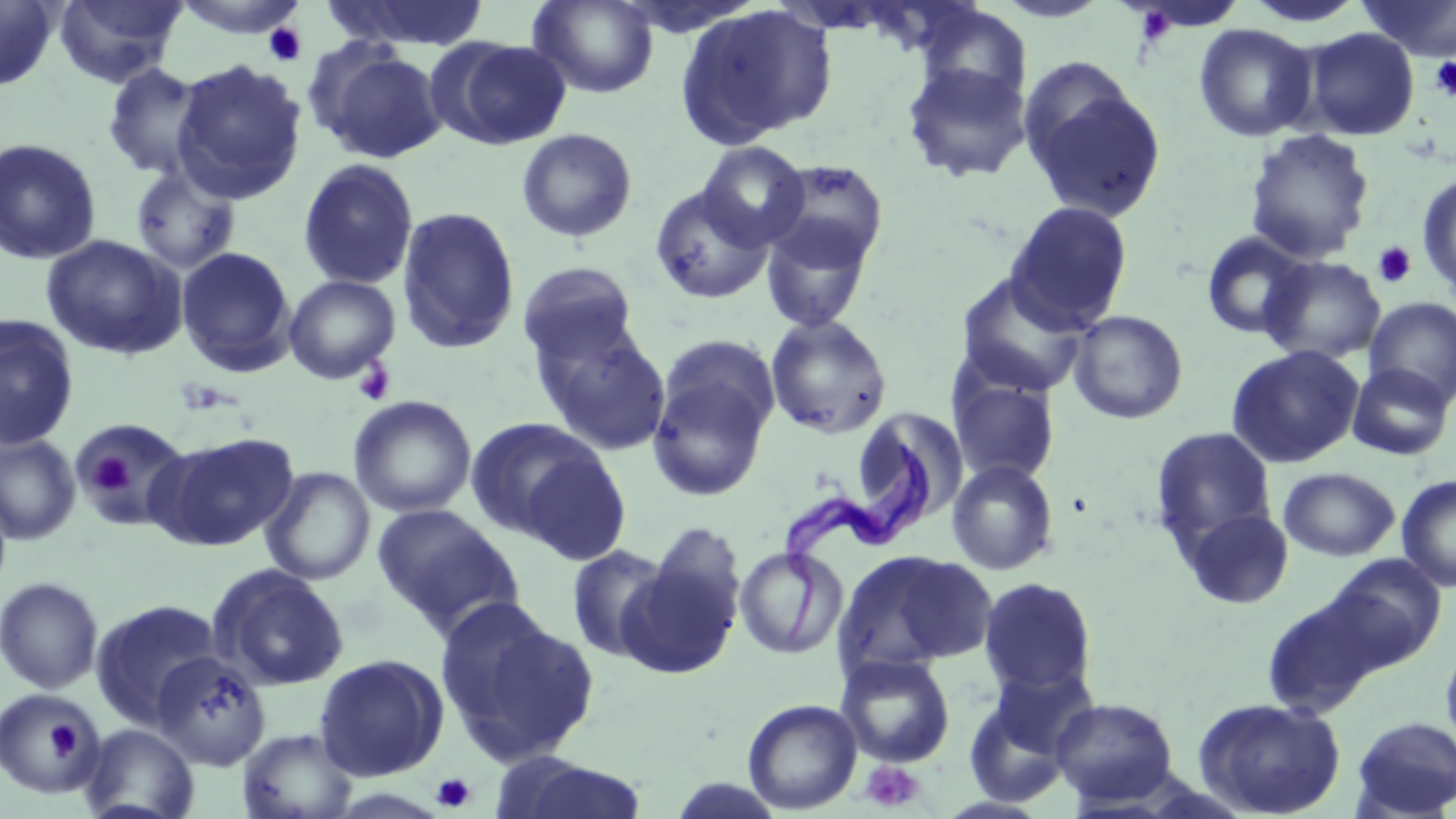

slide_level_diagnosis: Trypanosoma brucei
preparation: thin blood smear
uninfected_red_blood_cell_locations: 'approximate bounding boxes as named x1/y1/x2/y2 corners in pixels: (x1=0, y1=0, x2=59, y2=91), (x1=52, y1=0, x2=187, y2=88), (x1=170, y1=0, x2=311, y2=39), (x1=321, y1=0, x2=492, y2=51), (x1=527, y1=0, x2=659, y2=98), (x1=992, y1=0, x2=1111, y2=23), (x1=1243, y1=0, x2=1367, y2=29), (x1=1360, y1=0, x2=1456, y2=62), (x1=676, y1=3, x2=838, y2=148), (x1=915, y1=4, x2=1032, y2=106), (x1=1193, y1=24, x2=1318, y2=142), (x1=1297, y1=27, x2=1420, y2=141), (x1=440, y1=38, x2=572, y2=149), (x1=308, y1=42, x2=447, y2=164), (x1=172, y1=59, x2=307, y2=203), (x1=901, y1=62, x2=1032, y2=184), (x1=102, y1=63, x2=208, y2=181), (x1=1022, y1=79, x2=1166, y2=222), (x1=516, y1=128, x2=638, y2=243), (x1=1244, y1=128, x2=1375, y2=264), (x1=0, y1=138, x2=102, y2=265), (x1=697, y1=141, x2=811, y2=250), (x1=297, y1=159, x2=419, y2=290), (x1=764, y1=159, x2=890, y2=271), (x1=130, y1=165, x2=241, y2=275), (x1=1417, y1=172, x2=1456, y2=301), (x1=649, y1=184, x2=774, y2=305), (x1=1004, y1=200, x2=1133, y2=331), (x1=396, y1=206, x2=521, y2=355), (x1=759, y1=218, x2=875, y2=333), (x1=1200, y1=232, x2=1310, y2=339), (x1=41, y1=234, x2=187, y2=360), (x1=176, y1=246, x2=297, y2=377), (x1=1259, y1=256, x2=1387, y2=365), (x1=517, y1=262, x2=639, y2=364), (x1=955, y1=270, x2=1091, y2=398), (x1=284, y1=274, x2=400, y2=384), (x1=1364, y1=297, x2=1456, y2=408), (x1=1068, y1=309, x2=1189, y2=424), (x1=0, y1=315, x2=79, y2=450), (x1=765, y1=315, x2=892, y2=439), (x1=531, y1=321, x2=672, y2=455), (x1=1226, y1=344, x2=1365, y2=468), (x1=646, y1=357, x2=776, y2=503), (x1=1347, y1=363, x2=1454, y2=460), (x1=949, y1=377, x2=1061, y2=485), (x1=348, y1=395, x2=476, y2=518), (x1=850, y1=407, x2=967, y2=538), (x1=465, y1=417, x2=608, y2=542), (x1=72, y1=418, x2=195, y2=531), (x1=1150, y1=426, x2=1276, y2=555), (x1=150, y1=432, x2=299, y2=551), (x1=0, y1=433, x2=81, y2=545), (x1=516, y1=447, x2=635, y2=568), (x1=946, y1=459, x2=1060, y2=576), (x1=260, y1=467, x2=375, y2=585), (x1=1279, y1=467, x2=1400, y2=561), (x1=1396, y1=474, x2=1456, y2=593), (x1=371, y1=504, x2=525, y2=638), (x1=1180, y1=506, x2=1295, y2=610), (x1=566, y1=543, x2=677, y2=663), (x1=619, y1=543, x2=746, y2=681), (x1=734, y1=546, x2=846, y2=659), (x1=836, y1=549, x2=996, y2=674), (x1=1324, y1=553, x2=1447, y2=671), (x1=208, y1=565, x2=350, y2=692), (x1=0, y1=576, x2=103, y2=693), (x1=978, y1=577, x2=1098, y2=697), (x1=1260, y1=592, x2=1382, y2=718), (x1=435, y1=597, x2=596, y2=763), (x1=90, y1=599, x2=224, y2=730), (x1=1441, y1=637, x2=1456, y2=760), (x1=151, y1=651, x2=272, y2=770), (x1=313, y1=653, x2=449, y2=782), (x1=835, y1=653, x2=956, y2=768), (x1=960, y1=676, x2=1090, y2=806), (x1=1, y1=687, x2=106, y2=798), (x1=1192, y1=696, x2=1347, y2=818), (x1=1050, y1=697, x2=1179, y2=806), (x1=742, y1=698, x2=863, y2=814), (x1=1350, y1=716, x2=1456, y2=818), (x1=81, y1=724, x2=199, y2=819), (x1=238, y1=727, x2=359, y2=819), (x1=502, y1=756, x2=650, y2=819)'
field_of_view: one of a larger specimen
stain: May-Grünwald-Giemsa
magnification: 1000x
platelet_locations: 'approximate bounding boxes as named x1/y1/x2/y2 corners in pixels: (x1=1138, y1=8, x2=1173, y2=42), (x1=264, y1=23, x2=307, y2=66), (x1=1429, y1=56, x2=1456, y2=100), (x1=1373, y1=241, x2=1418, y2=288), (x1=353, y1=360, x2=396, y2=406), (x1=90, y1=455, x2=135, y2=495), (x1=41, y1=718, x2=85, y2=768), (x1=860, y1=760, x2=926, y2=813), (x1=431, y1=772, x2=476, y2=813)'
image_size: 1456×819 pixels
trypanosoma_brucei_locations: 'approximate bounding boxes as named x1/y1/x2/y2 corners in pixels: (x1=776, y1=430, x2=931, y2=643)'
modality: optical microscopy